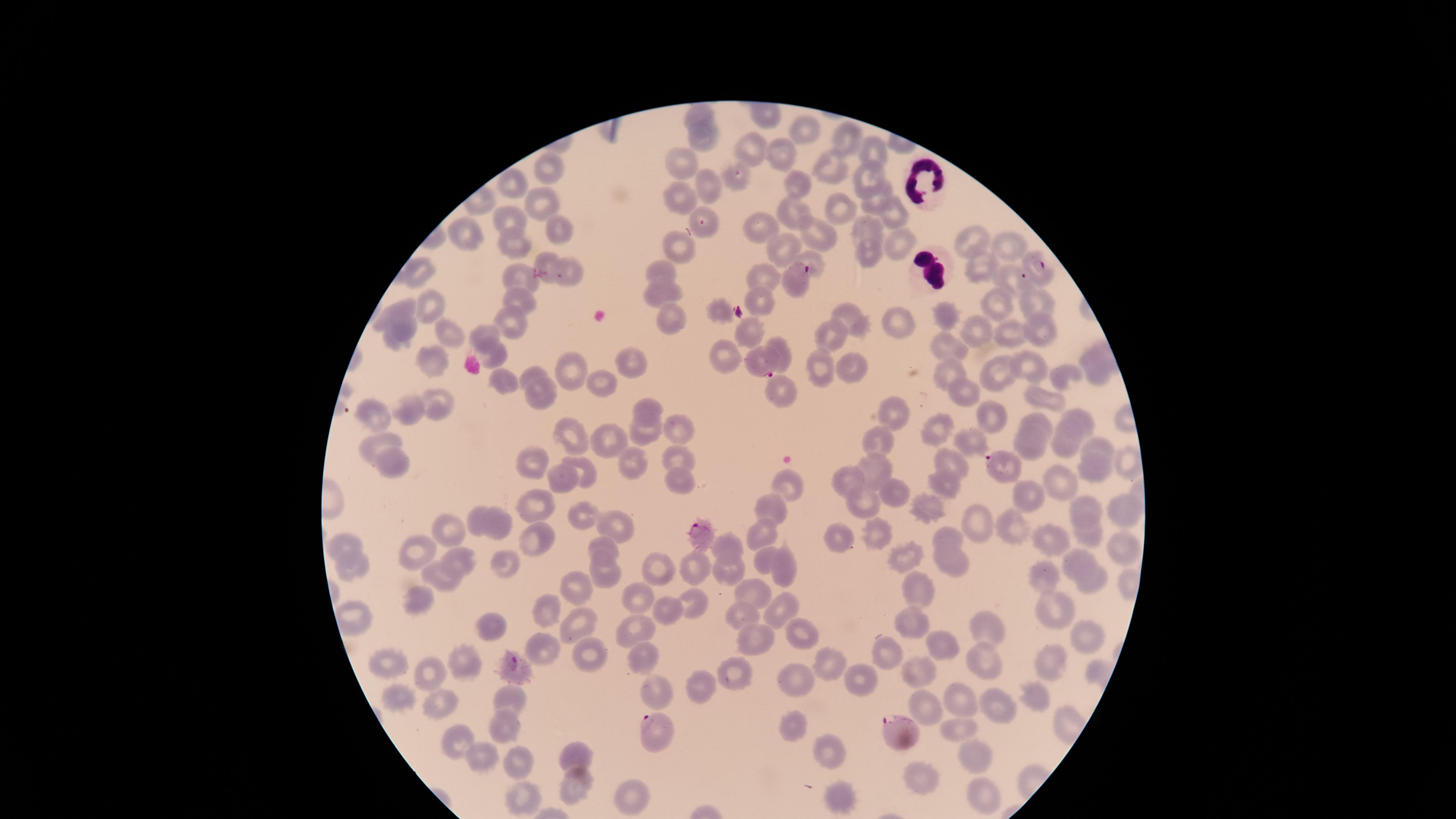 Approximate marker points as (x, y) in pixels. White blood cells: (922, 176), (926, 264). Parasitized red blood cells: (701, 221), (1042, 268), (562, 275), (795, 276), (1018, 278), (763, 365), (999, 462), (702, 534), (515, 662), (896, 728), (659, 735). Uninfected red blood cells: (702, 114), (807, 130), (703, 139), (847, 141), (754, 148), (780, 150), (878, 151), (681, 163), (830, 167), (546, 168), (867, 175), (732, 180), (797, 181), (709, 187), (517, 188), (872, 195), (677, 200), (541, 202), (837, 204), (788, 209), (898, 209), (510, 218), (760, 226), (868, 226), (557, 227), (469, 234), (822, 238), (511, 240), (896, 240), (972, 242), (1008, 243), (679, 244), (780, 249), (868, 251), (811, 258), (546, 262), (980, 267), (663, 269), (418, 272), (764, 279), (518, 280), (660, 289), (759, 298), (517, 300), (1036, 300), (431, 302), (996, 302), (396, 309), (719, 309), (847, 315), (671, 316), (950, 316), (894, 324), (1038, 324), (405, 325), (508, 327), (447, 330), (749, 330), (977, 332), (1014, 333), (484, 334), (833, 337), (948, 347), (777, 349), (494, 352), (723, 354), (630, 361), (426, 363), (568, 365), (1031, 366), (821, 367), (1097, 367), (949, 369), (851, 370), (532, 374), (992, 374), (1066, 378), (504, 380), (601, 383), (779, 389), (539, 392), (966, 393), (1049, 401), (439, 405), (408, 406), (645, 406), (372, 412), (896, 414), (989, 420), (1036, 420), (1080, 421), (681, 425), (1070, 427), (936, 430), (642, 432), (578, 438), (879, 439), (972, 439), (611, 440), (379, 444), (1029, 444), (1098, 447), (1064, 450), (1126, 459), (674, 461), (950, 461), (392, 462), (531, 463), (872, 464), (629, 466), (583, 469), (1094, 469), (563, 476), (1057, 479), (680, 480), (845, 482), (789, 485), (950, 486), (894, 489), (1028, 490), (536, 502), (865, 504), (766, 507), (1123, 508), (1089, 509), (926, 510), (581, 515), (480, 518), (616, 524), (1009, 526), (974, 527), (499, 528), (453, 529), (760, 529), (881, 534), (1087, 534), (533, 535), (1046, 536), (833, 537), (950, 539), (1118, 541), (346, 543), (725, 546), (601, 548), (417, 550), (1078, 555), (899, 558), (455, 559), (765, 559), (954, 562), (505, 564), (658, 567), (352, 569), (728, 570), (695, 571), (780, 571), (444, 574), (605, 574), (1040, 578), (1094, 583), (581, 586), (915, 588), (753, 593), (636, 594), (419, 595), (689, 602), (664, 605), (1057, 607), (545, 608), (778, 608), (746, 613), (351, 617), (910, 617), (486, 622), (579, 624), (634, 626), (983, 628), (800, 631), (754, 637), (1085, 640), (937, 643), (540, 646), (583, 653), (890, 655), (640, 656), (982, 657), (1057, 660), (463, 661), (828, 662), (389, 664), (427, 669), (915, 674), (735, 675), (801, 678), (858, 678), (703, 686), (661, 691), (1035, 695), (400, 697), (512, 699), (997, 699), (956, 702), (436, 704), (919, 705), (498, 726), (953, 726), (792, 728), (456, 739), (829, 751), (574, 754), (482, 756), (976, 756), (519, 761), (920, 780), (575, 784), (839, 796), (983, 797), (637, 799), (524, 800). Presence: malaria parasites identified. Giemsa stain. Species: Plasmodium falciparum. Image is 1456×819 pixels. Photographed with a smartphone camera through the microscope eyepiece. Single field of view. Circular visible region. Thin smear of blood.